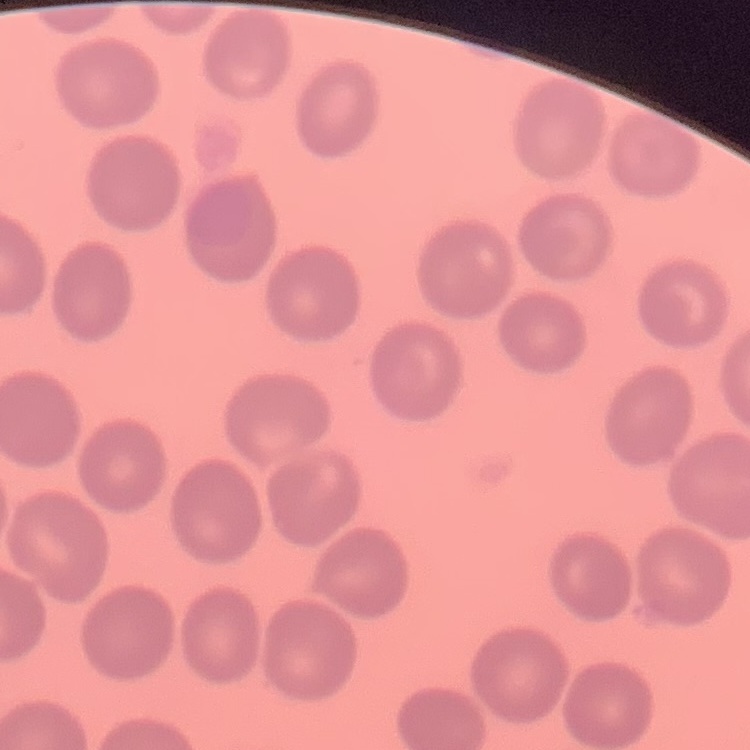
The erythrocytes show no rouleaux formation. Stained with either Field's or Giemsa. Thin blood film. One tile cut from a larger photomicrograph.